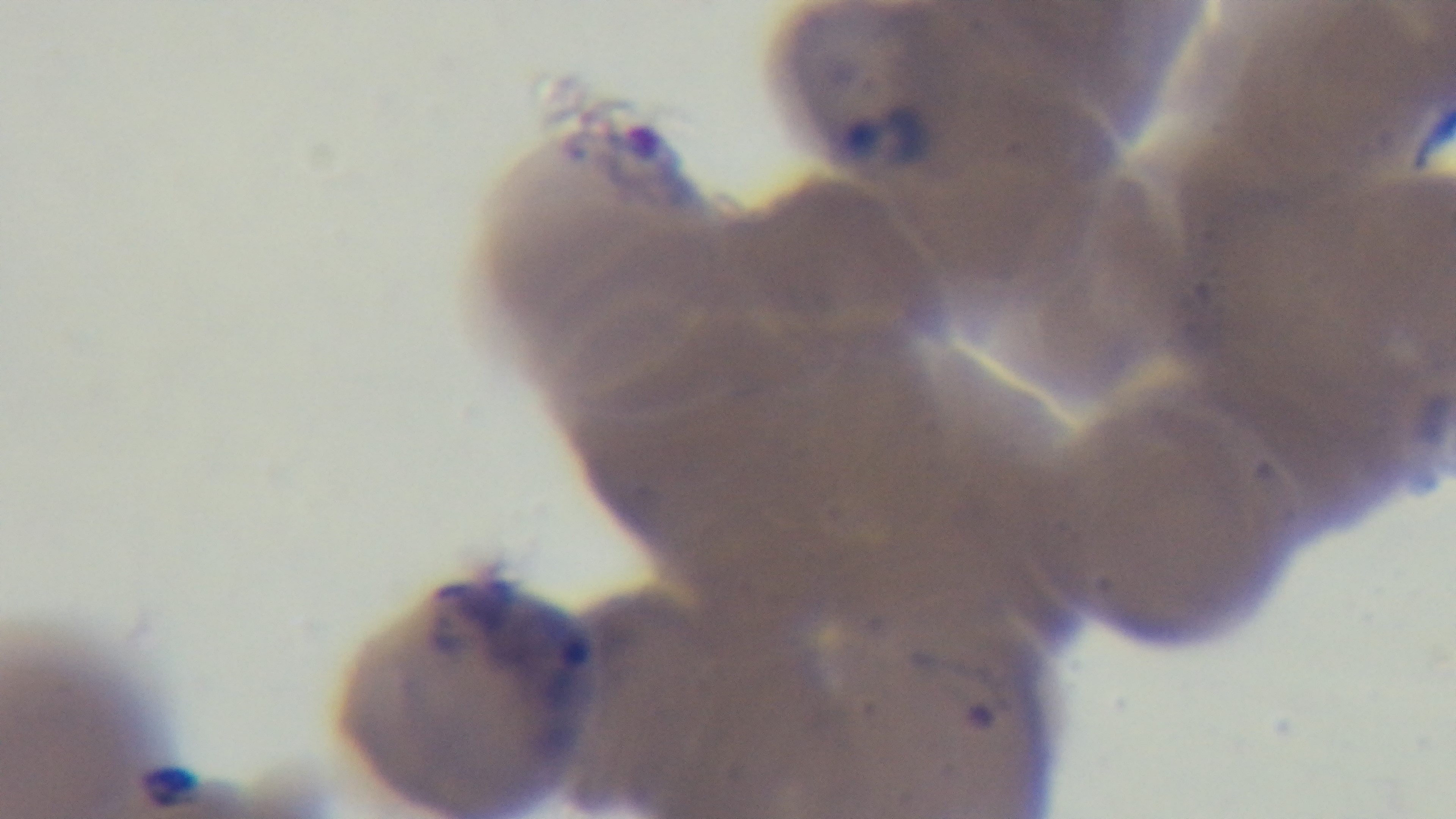 Preparation: thin smear. Malaria status: infected. Captured with a mounted 4K digital camera. Giemsa-stained. Photomicrograph. Single field of view. Oil-immersion objective, 100x.